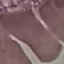

{
  "malaria_status": "uninfected",
  "capture": "smartphone through the microscope eyepiece",
  "image_type": "automatically extracted cell patch, resized to 64 × 64 pixels",
  "stain": "Giemsa",
  "preparation": "thin smear"
}